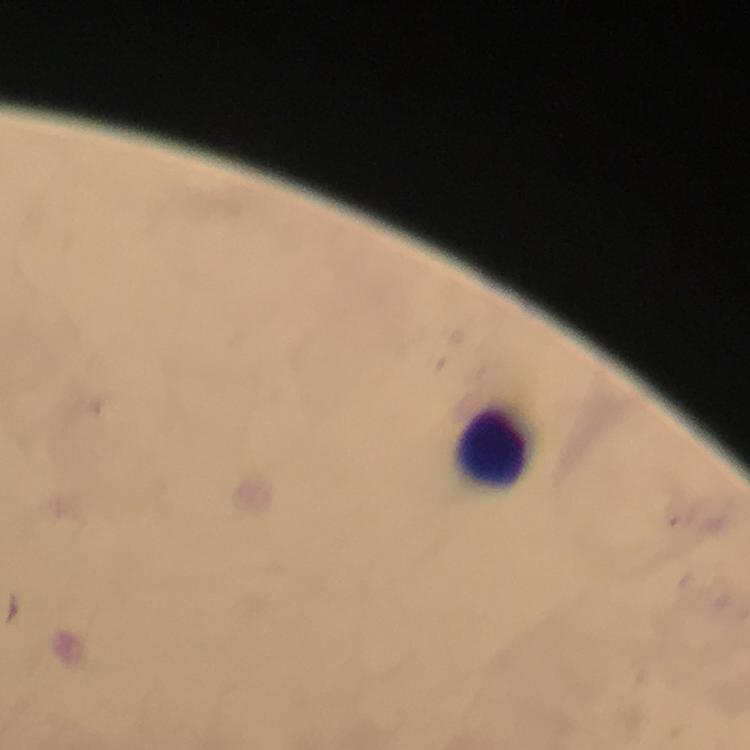

context = from a diagnostic examination for malaria
leukocyte locations = approximate centers as {x, y} in pixels: {492, 449}
immersion oil = applied
malaria parasites = none detected
magnification = 100x
image size = 750×750 pixels
preparation = thick smear
stain = Giemsa
cropped from = one field of view
capture = smartphone photograph through a microscope